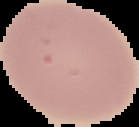 From a thin blood film. Segmented cell region on a black background. Image is 139×127 pixels. Result: negative for malaria parasites.